Identify the parasite.
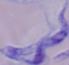

A trypanosome.

Captured at 1000x magnification. Micrograph.